Point out each leukocyte.
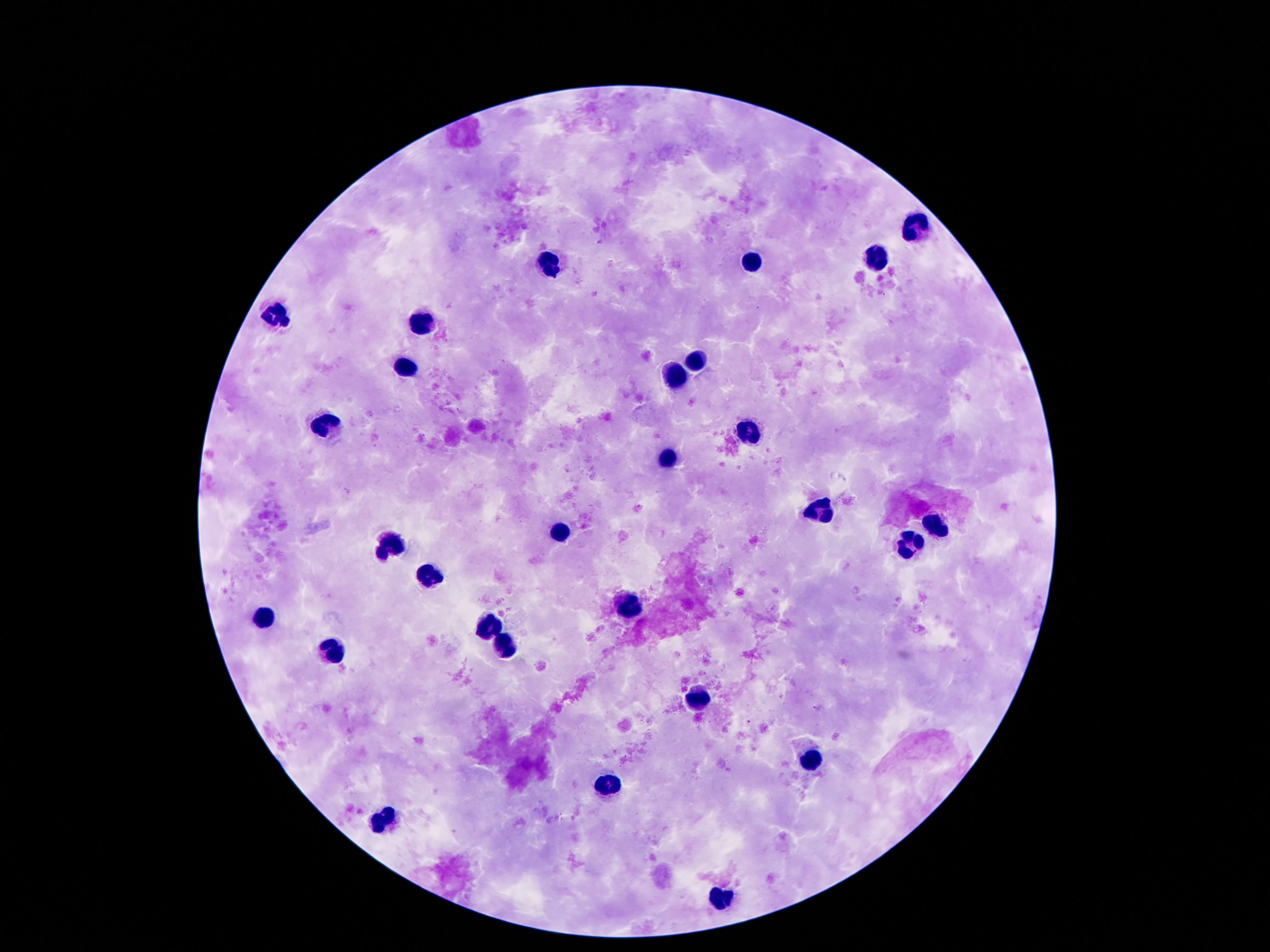

Approximate object centers, in pixels from the top-left corner.
Leukocytes: (x=919, y=226), (x=874, y=260), (x=551, y=262), (x=753, y=262), (x=274, y=309), (x=417, y=323), (x=694, y=363), (x=406, y=372), (x=673, y=377), (x=326, y=426), (x=746, y=430), (x=664, y=462), (x=822, y=512), (x=935, y=524), (x=561, y=533), (x=389, y=544), (x=910, y=544), (x=425, y=577), (x=631, y=611), (x=261, y=621), (x=490, y=626), (x=503, y=644), (x=335, y=652), (x=700, y=701), (x=811, y=760), (x=610, y=785), (x=381, y=822), (x=721, y=898).

Photographed through the microscope eyepiece with a smartphone camera. Thick peripheral-blood smear. Patient malaria status: negative. Image is 1270×952 pixels. Single field of view. 100x magnification. Giemsa stain.